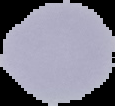 From a thin blood smear. Cell region segmented out of the field of view; the surrounding area is masked to black. Result: negative for Plasmodium parasites. Image is 115×106 pixels.